Outline each Plasmodium ovale-infected red blood cell.
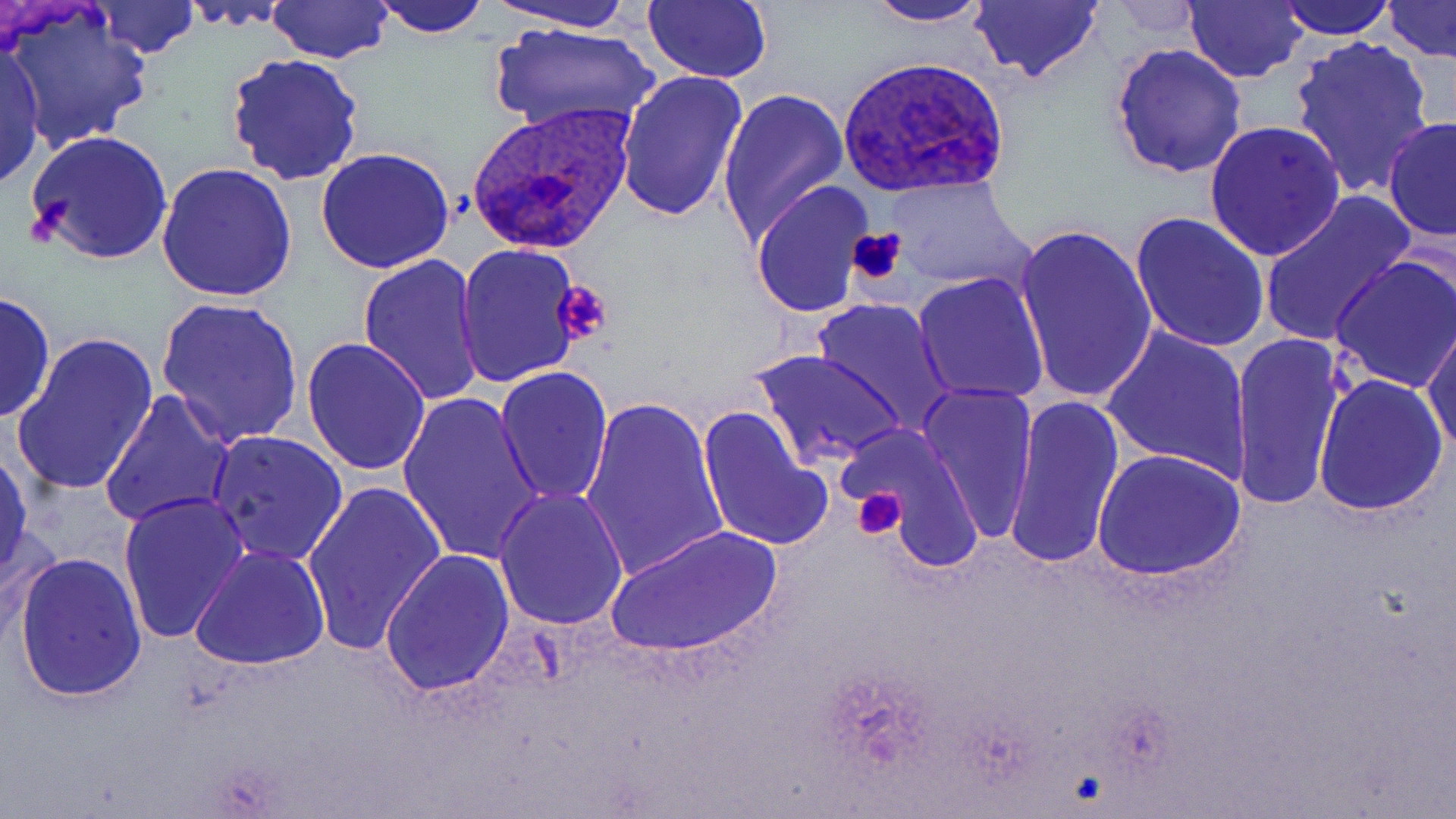
Approximate bounding boxes as (x1, y1, x2, y2) in pixels.
Plasmodium ovale-infected red blood cells: (838, 57, 1011, 195), (467, 105, 637, 253).

Platelet locations: (847, 226, 906, 287), (552, 279, 615, 345), (853, 489, 906, 540). Uninfected red blood cell locations: (1, 0, 156, 150), (267, 0, 394, 63), (374, 0, 492, 37), (490, 0, 637, 34), (643, 0, 772, 84), (1185, 0, 1308, 83), (1275, 0, 1399, 41), (1381, 0, 1455, 62), (89, 1, 199, 59), (858, 1, 994, 28), (968, 1, 1105, 85), (484, 21, 663, 139), (1288, 35, 1437, 196), (0, 42, 47, 194), (1110, 42, 1247, 179), (225, 51, 366, 185), (617, 70, 749, 222), (717, 86, 849, 247), (1382, 116, 1456, 243), (1205, 120, 1346, 259), (25, 128, 173, 267), (315, 146, 455, 274), (156, 164, 300, 304), (883, 175, 1029, 290), (750, 179, 877, 320), (1257, 192, 1416, 348), (1130, 210, 1271, 353), (1012, 219, 1157, 404), (454, 243, 585, 387), (356, 254, 488, 406), (1331, 256, 1456, 393), (911, 271, 1050, 406), (0, 291, 55, 425), (153, 297, 304, 448), (808, 297, 958, 437), (1423, 323, 1456, 455), (1097, 325, 1252, 480), (13, 331, 158, 497), (1227, 331, 1347, 514), (301, 336, 433, 476), (751, 346, 906, 470), (494, 365, 612, 507), (1313, 372, 1449, 517), (914, 380, 1040, 541), (99, 388, 236, 530), (396, 390, 546, 567), (1002, 393, 1125, 571), (579, 396, 730, 582), (697, 405, 833, 552), (842, 422, 986, 565), (206, 430, 348, 567), (0, 444, 34, 584), (1093, 447, 1246, 580), (301, 479, 446, 655), (493, 488, 628, 631), (117, 491, 250, 646), (1, 521, 65, 650), (605, 523, 781, 658), (190, 543, 330, 670), (379, 547, 514, 697), (13, 550, 148, 700). Slide-level diagnosis: Plasmodium ovale. Single field of view. May-Grünwald-Giemsa stain. Image is 1456×819 pixels. Light microscopy. 1000x magnification. Thin blood film.